Assess the morphology of the red blood cells.
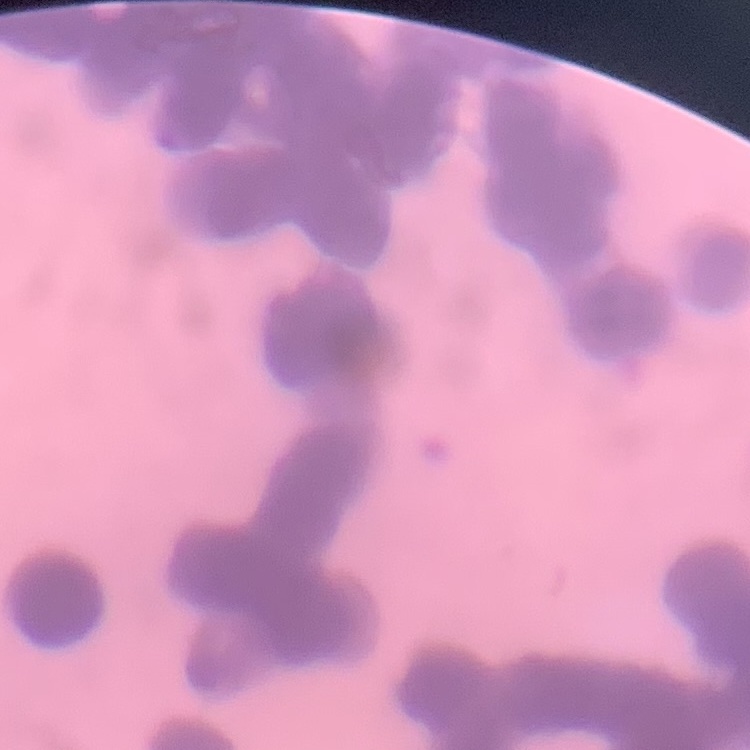

Rouleaux formation.

{
  "preparation": "thin peripheral smear",
  "stain": "Field's or Giemsa",
  "image_type": "square crop of a larger photomicrograph"
}